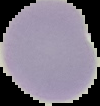
image type = segmented cell region with the area outside set to black
preparation = thin blood smear
result = negative for malaria parasites
image size = 100×106 pixels